Identify the parasite.
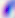
Toxoplasma gondii.

modality = photomicrograph
magnification = 400x